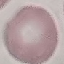

malaria status = uninfected
stain = Giemsa
image type = automatically extracted cell patch, resized to 64 × 64 pixels
preparation = thin smear
capture = smartphone through the microscope eyepiece